Identify the blood parasite species.
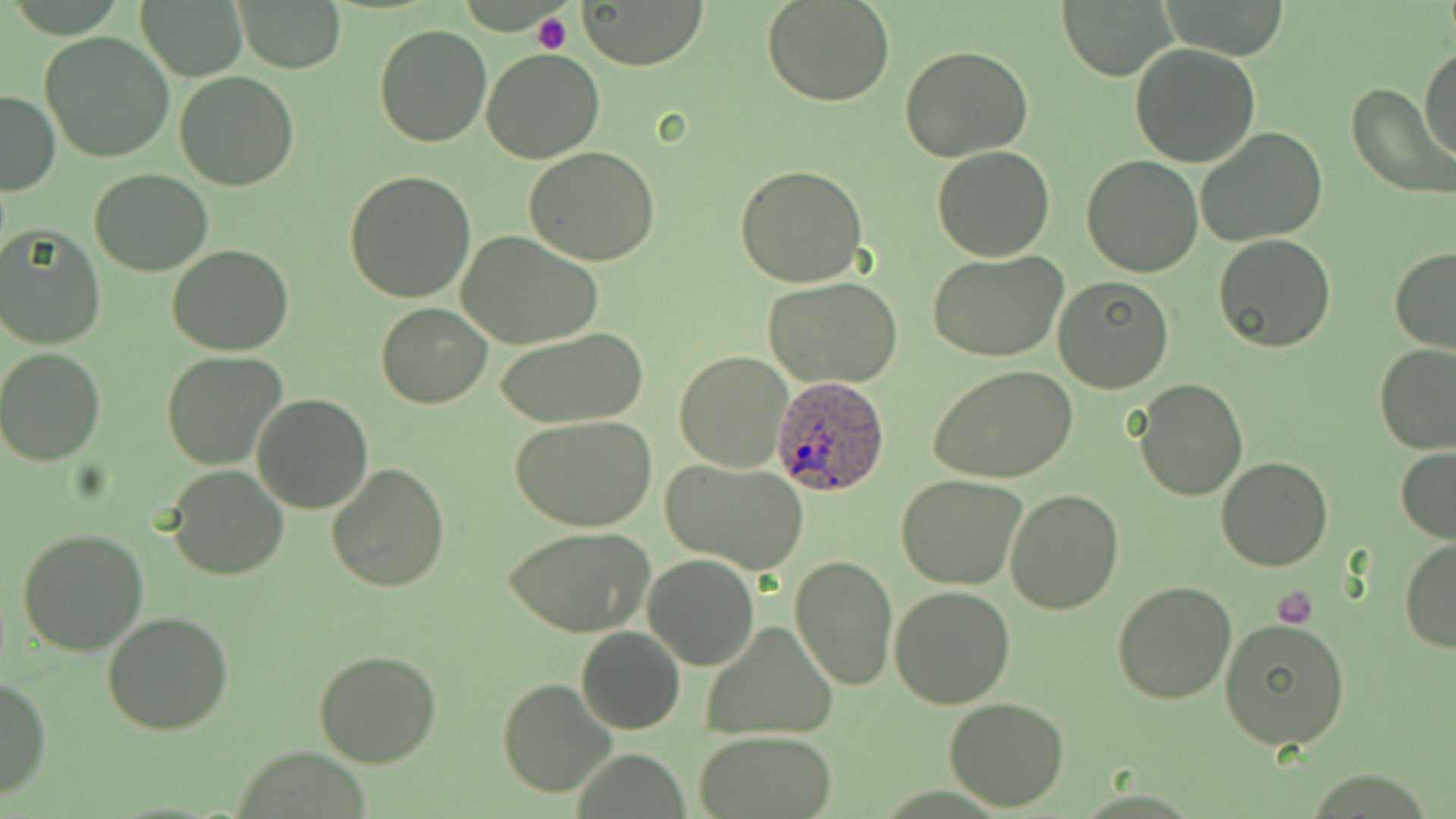
Plasmodium ovale.

modality = light microscopy
Plasmodium ovale-infected red blood cell locations = approximate bounding boxes as named x1/y1/x2/y2 corners in pixels: (x1=771, y1=374, x2=890, y2=497)
image size = 1456×819 pixels
magnification = 1000x
preparation = thin blood smear
platelet locations = approximate bounding boxes as named x1/y1/x2/y2 corners in pixels: (x1=533, y1=12, x2=573, y2=55), (x1=1273, y1=586, x2=1318, y2=629)
stain = May-Grünwald-Giemsa
field of view = one of a larger specimen
uninfected red blood cell locations = approximate bounding boxes as named x1/y1/x2/y2 corners in pixels: (x1=762, y1=0, x2=896, y2=107), (x1=233, y1=1, x2=345, y2=73), (x1=581, y1=1, x2=705, y2=70), (x1=139, y1=2, x2=246, y2=80), (x1=1059, y1=2, x2=1174, y2=79), (x1=372, y1=25, x2=494, y2=149), (x1=40, y1=31, x2=175, y2=161), (x1=1420, y1=42, x2=1456, y2=163), (x1=1130, y1=44, x2=1262, y2=168), (x1=901, y1=45, x2=1032, y2=164), (x1=481, y1=47, x2=604, y2=163), (x1=174, y1=72, x2=301, y2=191), (x1=1346, y1=84, x2=1456, y2=199), (x1=0, y1=88, x2=59, y2=197), (x1=1195, y1=128, x2=1328, y2=247), (x1=525, y1=144, x2=661, y2=264), (x1=931, y1=145, x2=1056, y2=262), (x1=1082, y1=155, x2=1202, y2=277), (x1=734, y1=164, x2=868, y2=288), (x1=88, y1=168, x2=213, y2=276), (x1=344, y1=171, x2=477, y2=302), (x1=0, y1=223, x2=106, y2=349), (x1=456, y1=230, x2=602, y2=349), (x1=1212, y1=234, x2=1337, y2=354), (x1=167, y1=245, x2=294, y2=355), (x1=1389, y1=247, x2=1456, y2=353), (x1=929, y1=251, x2=1067, y2=362), (x1=928, y1=266, x2=1174, y2=380), (x1=1052, y1=276, x2=1173, y2=394), (x1=763, y1=278, x2=903, y2=387), (x1=375, y1=303, x2=493, y2=407), (x1=495, y1=327, x2=650, y2=428), (x1=1373, y1=343, x2=1455, y2=454), (x1=0, y1=349, x2=104, y2=465), (x1=160, y1=351, x2=287, y2=470), (x1=675, y1=351, x2=795, y2=473), (x1=929, y1=365, x2=1078, y2=483), (x1=1132, y1=377, x2=1249, y2=502), (x1=252, y1=393, x2=375, y2=513), (x1=510, y1=414, x2=657, y2=531), (x1=1396, y1=447, x2=1456, y2=544), (x1=1215, y1=457, x2=1333, y2=572), (x1=662, y1=459, x2=810, y2=574), (x1=326, y1=462, x2=452, y2=593), (x1=165, y1=466, x2=288, y2=581), (x1=897, y1=473, x2=1027, y2=590), (x1=1005, y1=487, x2=1124, y2=613), (x1=505, y1=526, x2=652, y2=639), (x1=16, y1=528, x2=150, y2=656), (x1=1399, y1=539, x2=1456, y2=652), (x1=643, y1=555, x2=759, y2=670), (x1=790, y1=555, x2=897, y2=690), (x1=1113, y1=579, x2=1237, y2=703), (x1=890, y1=586, x2=1015, y2=708), (x1=103, y1=610, x2=234, y2=735), (x1=1220, y1=620, x2=1349, y2=751), (x1=701, y1=621, x2=837, y2=739), (x1=576, y1=626, x2=685, y2=734), (x1=313, y1=647, x2=441, y2=769), (x1=0, y1=676, x2=51, y2=802), (x1=497, y1=678, x2=618, y2=800), (x1=943, y1=695, x2=1068, y2=811), (x1=697, y1=731, x2=837, y2=818)